State which parasite is depicted.
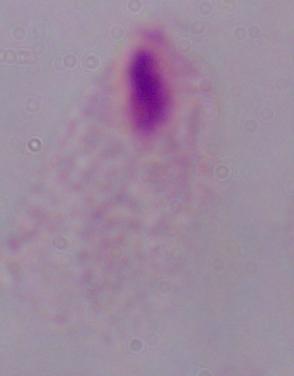
A trichomonad.

1000x magnification. Photomicrograph.